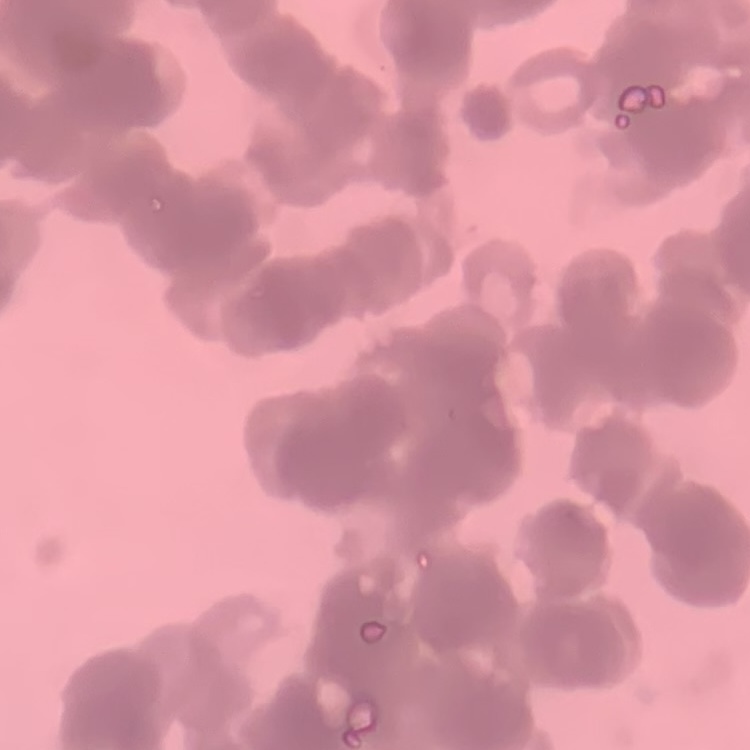

erythrocyte morphology = rouleaux formation
stain = Field's or Giemsa
preparation = thin peripheral smear
image type = square crop of a larger photomicrograph